Describe the morphology of the erythrocytes.
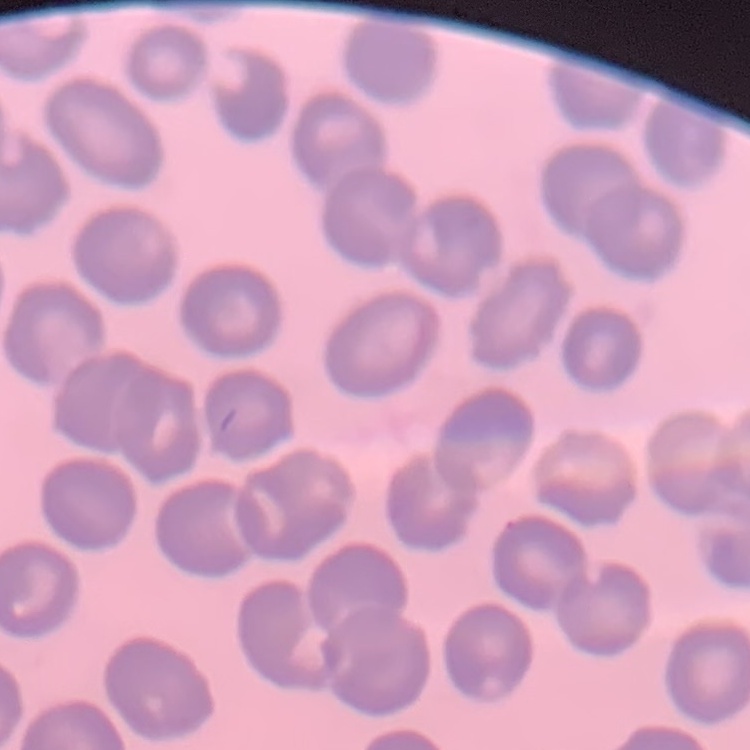
They show no rouleaux formation.

preparation = thin peripheral smear
stain = Field's or Giemsa
image type = square crop of a larger photomicrograph